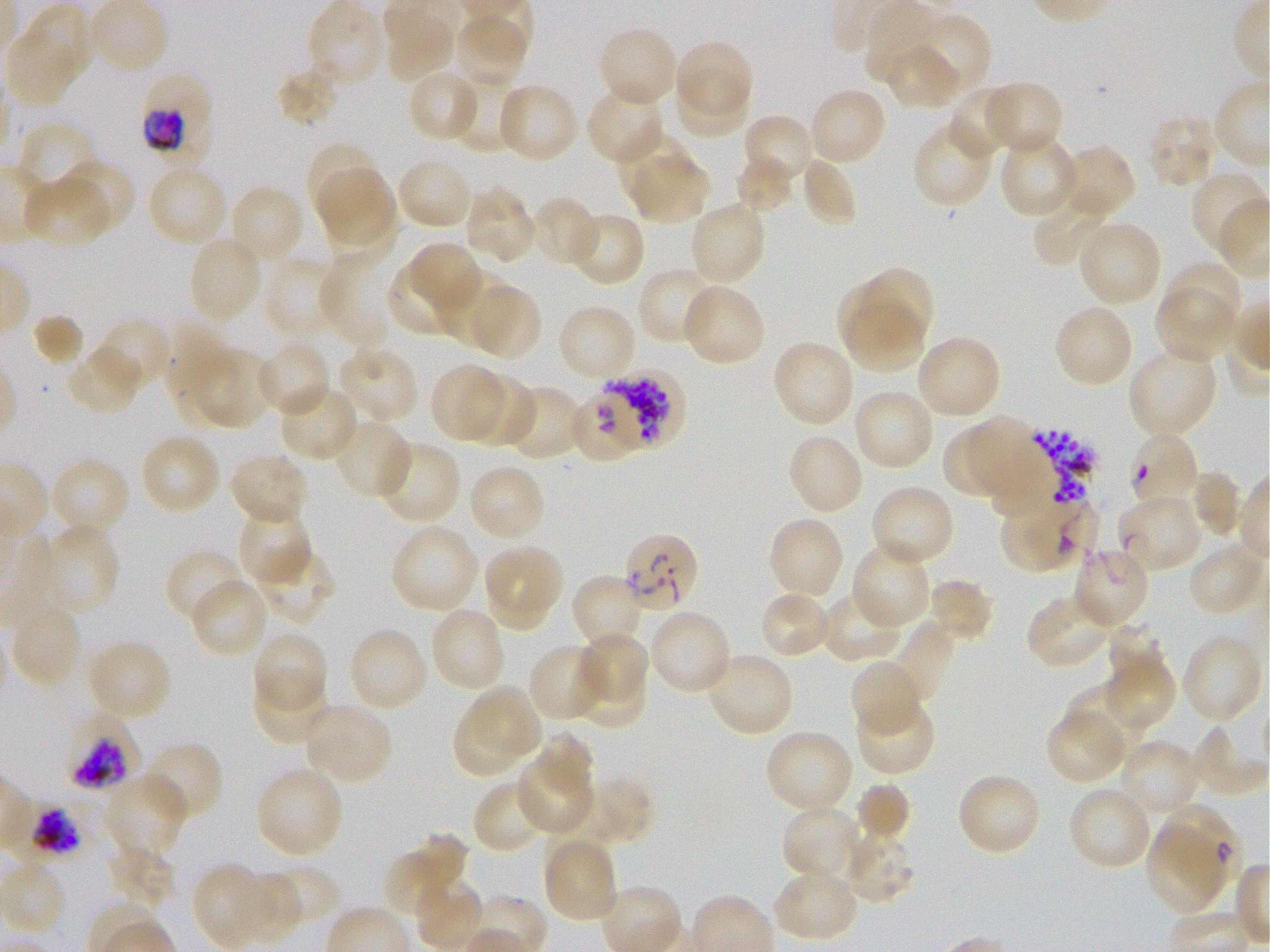
Approximate bounding rectangles given as corner coordinates in pixels from the top-left. Not every red blood cell is marked. A life-cycle stage — or a range of stages, where the recorded stages span more than one — follows each staged infected red blood cell.
Summary:
  - Locations of infected red blood cells: (x1=138, y1=71, x2=212, y2=158) trophozoite; (x1=1129, y1=434, x2=1202, y2=506); (x1=1114, y1=493, x2=1201, y2=574); (x1=622, y1=535, x2=699, y2=613); (x1=64, y1=712, x2=141, y2=792) late trophozoite to early schizont; (x1=4, y1=794, x2=81, y2=875) trophozoite
  - Locations of red blood cells of indeterminate infection status: (x1=563, y1=387, x2=649, y2=465), (x1=998, y1=496, x2=1098, y2=574), (x1=1167, y1=801, x2=1242, y2=884)
  - Locations of uninfected red blood cells: (x1=7, y1=6, x2=95, y2=105), (x1=381, y1=13, x2=454, y2=84), (x1=453, y1=18, x2=532, y2=89), (x1=916, y1=18, x2=988, y2=90), (x1=596, y1=25, x2=680, y2=109), (x1=672, y1=39, x2=753, y2=111), (x1=881, y1=45, x2=961, y2=112), (x1=277, y1=67, x2=340, y2=126), (x1=405, y1=68, x2=480, y2=143), (x1=676, y1=70, x2=746, y2=139), (x1=450, y1=72, x2=523, y2=151), (x1=980, y1=79, x2=1065, y2=156), (x1=496, y1=83, x2=579, y2=165), (x1=585, y1=85, x2=665, y2=165), (x1=947, y1=85, x2=1022, y2=159), (x1=807, y1=86, x2=888, y2=167), (x1=1146, y1=112, x2=1218, y2=190), (x1=741, y1=113, x2=816, y2=188), (x1=912, y1=119, x2=996, y2=208), (x1=14, y1=120, x2=96, y2=190), (x1=998, y1=132, x2=1078, y2=220), (x1=616, y1=133, x2=690, y2=197), (x1=308, y1=144, x2=381, y2=213), (x1=1053, y1=144, x2=1136, y2=222), (x1=734, y1=153, x2=797, y2=214), (x1=800, y1=154, x2=858, y2=228), (x1=395, y1=155, x2=476, y2=232), (x1=629, y1=157, x2=708, y2=222), (x1=56, y1=160, x2=135, y2=236), (x1=146, y1=164, x2=229, y2=248), (x1=317, y1=166, x2=394, y2=247), (x1=1191, y1=170, x2=1268, y2=259), (x1=23, y1=175, x2=111, y2=249), (x1=227, y1=184, x2=304, y2=267), (x1=463, y1=185, x2=537, y2=265), (x1=1033, y1=192, x2=1110, y2=265), (x1=330, y1=196, x2=405, y2=258), (x1=528, y1=196, x2=600, y2=268), (x1=687, y1=201, x2=767, y2=288), (x1=564, y1=211, x2=646, y2=288), (x1=1076, y1=219, x2=1163, y2=309), (x1=188, y1=236, x2=264, y2=325), (x1=411, y1=242, x2=483, y2=308), (x1=318, y1=247, x2=404, y2=347), (x1=263, y1=258, x2=343, y2=339), (x1=1174, y1=262, x2=1242, y2=327), (x1=390, y1=263, x2=460, y2=336), (x1=636, y1=266, x2=719, y2=346), (x1=859, y1=267, x2=933, y2=347), (x1=434, y1=268, x2=514, y2=348), (x1=837, y1=283, x2=910, y2=355), (x1=475, y1=284, x2=542, y2=360), (x1=681, y1=284, x2=765, y2=368), (x1=1154, y1=286, x2=1237, y2=363), (x1=556, y1=303, x2=638, y2=384), (x1=1053, y1=303, x2=1135, y2=389), (x1=846, y1=304, x2=927, y2=371), (x1=32, y1=313, x2=83, y2=367), (x1=93, y1=318, x2=172, y2=395), (x1=914, y1=334, x2=1002, y2=421), (x1=771, y1=338, x2=856, y2=429), (x1=255, y1=340, x2=331, y2=418), (x1=182, y1=344, x2=274, y2=431), (x1=66, y1=345, x2=144, y2=416), (x1=334, y1=345, x2=420, y2=425), (x1=1126, y1=345, x2=1220, y2=439), (x1=429, y1=363, x2=511, y2=442), (x1=462, y1=372, x2=535, y2=448), (x1=277, y1=382, x2=361, y2=463), (x1=503, y1=383, x2=588, y2=461), (x1=852, y1=388, x2=935, y2=472), (x1=970, y1=417, x2=1034, y2=497), (x1=333, y1=418, x2=413, y2=501), (x1=941, y1=424, x2=1008, y2=494), (x1=786, y1=432, x2=864, y2=517), (x1=138, y1=433, x2=221, y2=516), (x1=372, y1=440, x2=461, y2=526), (x1=228, y1=452, x2=311, y2=526), (x1=49, y1=456, x2=131, y2=538), (x1=467, y1=463, x2=547, y2=544), (x1=1189, y1=470, x2=1242, y2=538), (x1=869, y1=484, x2=956, y2=569), (x1=235, y1=507, x2=313, y2=587), (x1=766, y1=516, x2=845, y2=603), (x1=36, y1=523, x2=119, y2=619), (x1=390, y1=524, x2=480, y2=616), (x1=1187, y1=540, x2=1268, y2=616), (x1=850, y1=541, x2=931, y2=631), (x1=481, y1=542, x2=564, y2=633), (x1=1071, y1=544, x2=1149, y2=630), (x1=165, y1=547, x2=246, y2=626), (x1=250, y1=547, x2=339, y2=626), (x1=570, y1=573, x2=646, y2=652), (x1=189, y1=577, x2=269, y2=659), (x1=925, y1=577, x2=995, y2=643), (x1=818, y1=590, x2=907, y2=664), (x1=757, y1=591, x2=833, y2=661), (x1=1025, y1=593, x2=1113, y2=670), (x1=8, y1=604, x2=84, y2=689), (x1=429, y1=606, x2=506, y2=694), (x1=648, y1=608, x2=733, y2=696), (x1=881, y1=615, x2=958, y2=710), (x1=1107, y1=621, x2=1165, y2=671), (x1=346, y1=626, x2=430, y2=714), (x1=251, y1=631, x2=327, y2=717), (x1=580, y1=633, x2=649, y2=700), (x1=1180, y1=634, x2=1263, y2=725), (x1=85, y1=638, x2=173, y2=721), (x1=528, y1=643, x2=610, y2=723), (x1=704, y1=650, x2=795, y2=738), (x1=1100, y1=653, x2=1176, y2=732), (x1=851, y1=660, x2=923, y2=737), (x1=573, y1=665, x2=644, y2=727), (x1=252, y1=671, x2=330, y2=744), (x1=475, y1=683, x2=543, y2=760), (x1=1064, y1=689, x2=1150, y2=746), (x1=854, y1=694, x2=935, y2=776), (x1=300, y1=703, x2=393, y2=786), (x1=452, y1=705, x2=511, y2=779), (x1=1045, y1=709, x2=1128, y2=784), (x1=1192, y1=727, x2=1268, y2=794), (x1=762, y1=728, x2=855, y2=816), (x1=536, y1=732, x2=596, y2=791), (x1=1118, y1=738, x2=1202, y2=816), (x1=140, y1=740, x2=224, y2=823), (x1=515, y1=761, x2=590, y2=837), (x1=254, y1=764, x2=345, y2=859), (x1=103, y1=772, x2=189, y2=862), (x1=956, y1=772, x2=1041, y2=857), (x1=569, y1=777, x2=653, y2=846), (x1=855, y1=781, x2=912, y2=843), (x1=472, y1=782, x2=553, y2=855), (x1=1067, y1=784, x2=1154, y2=871), (x1=781, y1=804, x2=864, y2=885), (x1=1148, y1=826, x2=1223, y2=909), (x1=838, y1=829, x2=913, y2=904), (x1=541, y1=835, x2=619, y2=925), (x1=383, y1=837, x2=468, y2=924), (x1=107, y1=840, x2=177, y2=910), (x1=275, y1=864, x2=341, y2=917), (x1=195, y1=865, x2=261, y2=947), (x1=772, y1=867, x2=859, y2=944), (x1=245, y1=870, x2=304, y2=938), (x1=410, y1=878, x2=484, y2=952)
  - Stain: Giemsa
  - Preparation: thin blood film
  - Objective: 100x, oil immersion, numerical aperture 1.25
  - Field of view: single
  - Culture: in-vitro P. falciparum strain 3D7, static
  - Image size: 1270×952 pixels
  - Donor blood group: O+